Outline each Plasmodium vivax-infected red blood cell.
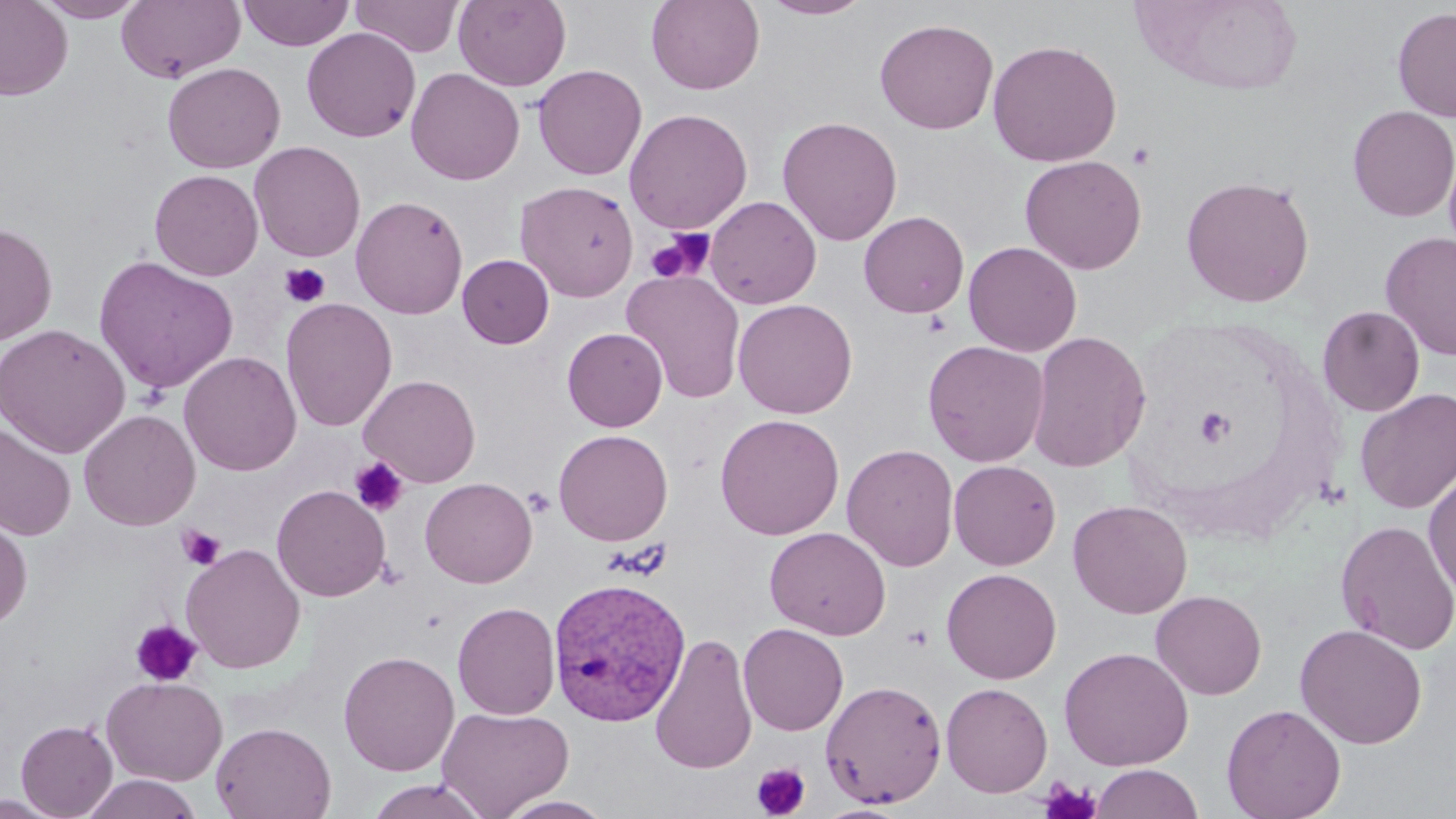
Approximate bounding boxes as (x1, y1, x2, y2) in pixels.
Plasmodium vivax-infected red blood cells: (547, 576, 691, 727).

Platelet locations: (1128, 142, 1156, 171), (645, 229, 712, 285), (280, 262, 330, 308), (1195, 405, 1235, 447), (350, 457, 409, 517), (523, 486, 555, 517), (177, 525, 225, 569), (130, 619, 202, 687), (751, 763, 811, 818), (1038, 778, 1101, 819). Uninfected red blood cell locations: (0, 0, 73, 101), (33, 0, 149, 22), (237, 0, 355, 51), (349, 0, 464, 57), (454, 0, 571, 91), (646, 0, 765, 94), (758, 0, 875, 20), (116, 1, 245, 83), (1392, 6, 1456, 122), (874, 18, 999, 134), (301, 27, 420, 142), (986, 39, 1123, 167), (162, 62, 285, 173), (532, 64, 647, 180), (406, 67, 524, 186), (1347, 105, 1456, 222), (624, 108, 753, 234), (777, 115, 903, 246), (248, 141, 365, 262), (1020, 154, 1147, 275), (149, 169, 263, 281), (1181, 175, 1315, 308), (515, 180, 639, 301), (351, 195, 468, 319), (705, 196, 821, 309), (859, 210, 969, 318), (0, 222, 58, 346), (1381, 232, 1456, 360), (963, 241, 1082, 357), (457, 254, 554, 349), (93, 256, 239, 395), (621, 269, 746, 404), (280, 297, 397, 432), (732, 298, 858, 418), (1317, 305, 1425, 417), (0, 323, 130, 458), (562, 327, 668, 431), (1027, 330, 1151, 473), (923, 340, 1050, 467), (178, 351, 302, 477), (359, 374, 481, 487), (1354, 387, 1456, 514), (79, 409, 200, 531), (714, 413, 844, 540), (0, 423, 77, 541), (553, 428, 673, 545), (842, 443, 959, 571), (948, 459, 1061, 570), (1423, 468, 1456, 600), (420, 477, 537, 588), (271, 484, 391, 602), (1068, 499, 1192, 618), (0, 510, 33, 629), (1335, 520, 1456, 655), (765, 526, 891, 640), (181, 543, 306, 674), (941, 567, 1062, 684), (1151, 589, 1267, 700), (452, 601, 561, 720), (738, 622, 849, 736), (1294, 623, 1428, 749), (650, 632, 758, 774), (1058, 646, 1194, 771), (338, 650, 459, 776), (101, 676, 227, 786), (820, 679, 947, 808), (941, 682, 1053, 797), (1221, 703, 1347, 819), (437, 706, 575, 818), (16, 719, 117, 818), (210, 722, 336, 819), (1090, 763, 1204, 819), (79, 774, 203, 819), (366, 778, 493, 818), (0, 792, 66, 819), (496, 795, 618, 818). Slide-level diagnosis: Plasmodium vivax. Optical microscopy. Single field of view. May-Grünwald-Giemsa stain. Image is 1456×819 pixels. Thin blood smear. Captured at 1000x magnification.